Assess this cell for malaria.
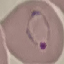
It is parasitized.

Photographed with a smartphone camera at the microscope eyepiece. Giemsa stain. Thin smear of blood. Cell patch, automatically extracted from a larger field of view and resized to 64 × 64 pixels.